Locate every blood parasite and identify its species.
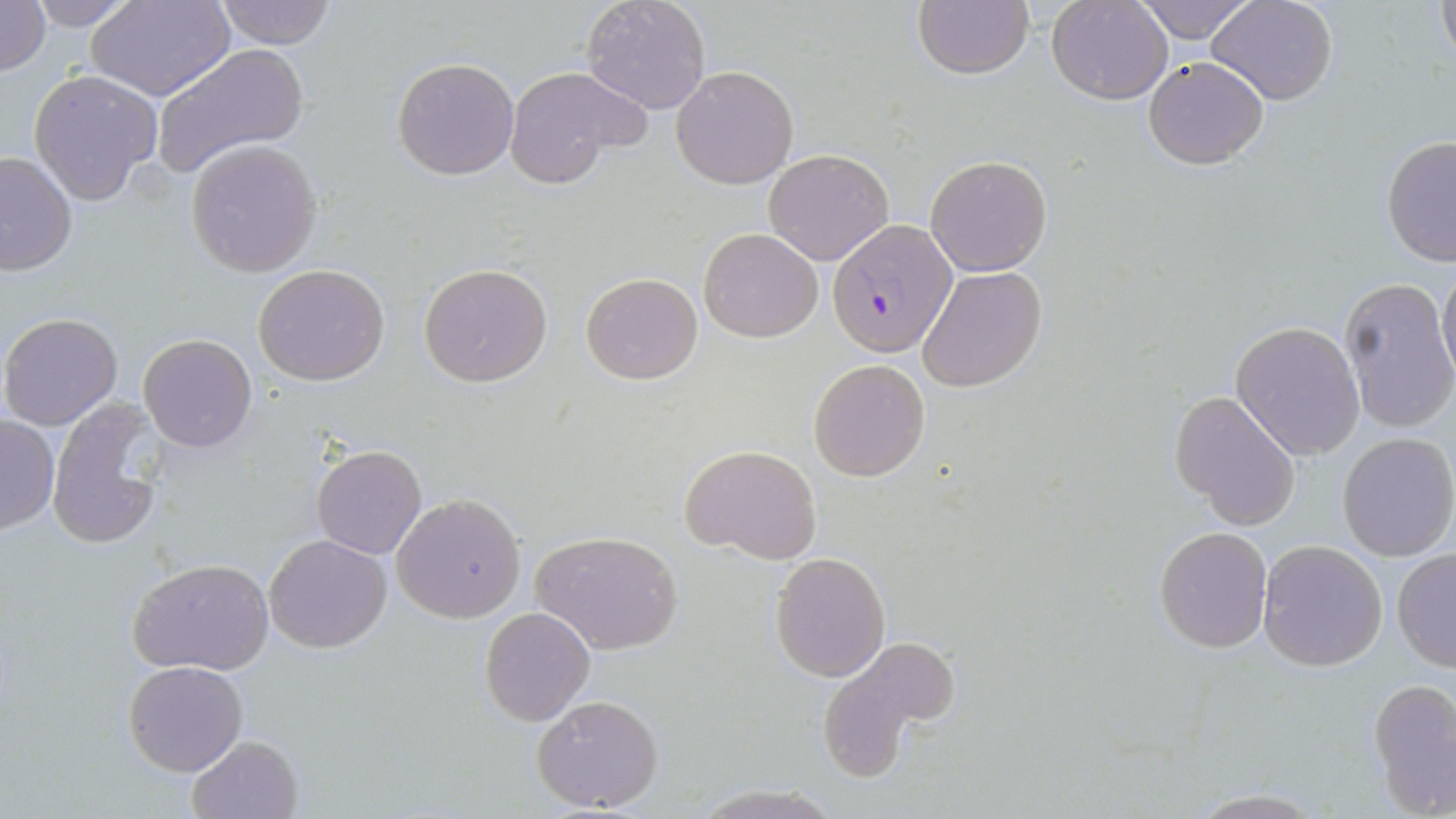

Approximate bounding boxes as (x1, y1, x2, y2) in pixels.
Plasmodium falciparum-infected red blood cells: (827, 219, 957, 356).
No Plasmodium ovale, Plasmodium malariae, Plasmodium vivax, Babesia divergens, or Trypanosoma brucei observed.

slide-level diagnosis = Plasmodium falciparum
image size = 1456×819 pixels
modality = light microscopy
uninfected red blood cell locations = approximate bounding boxes as (x1, y1, x2, y2) in pixels: (0, 0, 50, 78), (25, 0, 140, 29), (211, 0, 337, 49), (581, 0, 712, 115), (912, 0, 1035, 80), (1047, 0, 1172, 104), (1132, 0, 1257, 44), (1208, 0, 1338, 106), (1434, 0, 1455, 69), (88, 1, 234, 101), (149, 43, 308, 179), (1144, 55, 1269, 168), (392, 57, 519, 180), (503, 65, 648, 190), (671, 65, 800, 189), (28, 70, 164, 204), (1380, 135, 1456, 269), (186, 141, 322, 277), (764, 148, 893, 265), (0, 149, 77, 275), (924, 154, 1052, 275), (699, 227, 824, 342), (418, 262, 552, 389), (1438, 262, 1456, 384), (253, 263, 391, 386), (918, 266, 1045, 394), (581, 272, 702, 385), (1340, 278, 1456, 433), (0, 312, 123, 430), (1231, 321, 1365, 460), (138, 334, 257, 452), (808, 359, 929, 481), (1169, 392, 1302, 530), (47, 396, 174, 551), (0, 415, 58, 534), (1336, 433, 1456, 559), (682, 443, 823, 565), (311, 444, 427, 559), (392, 493, 526, 622), (1154, 527, 1271, 652), (531, 531, 683, 655), (262, 533, 393, 653), (1258, 541, 1387, 670), (1391, 550, 1456, 672), (770, 552, 890, 681), (128, 558, 274, 677), (480, 607, 596, 727), (814, 636, 959, 779), (123, 659, 247, 776), (1368, 678, 1456, 816), (531, 693, 664, 813), (186, 735, 305, 819), (1187, 790, 1328, 817)
field of view = single
stain = May-Grünwald-Giemsa
magnification = 1000x
preparation = thin blood smear